State which parasite is depicted.
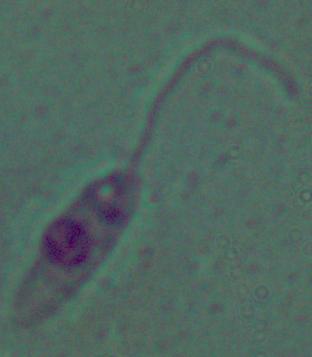

Leishmania.

Summary:
  - Magnification: 1000x
  - Modality: photomicrograph